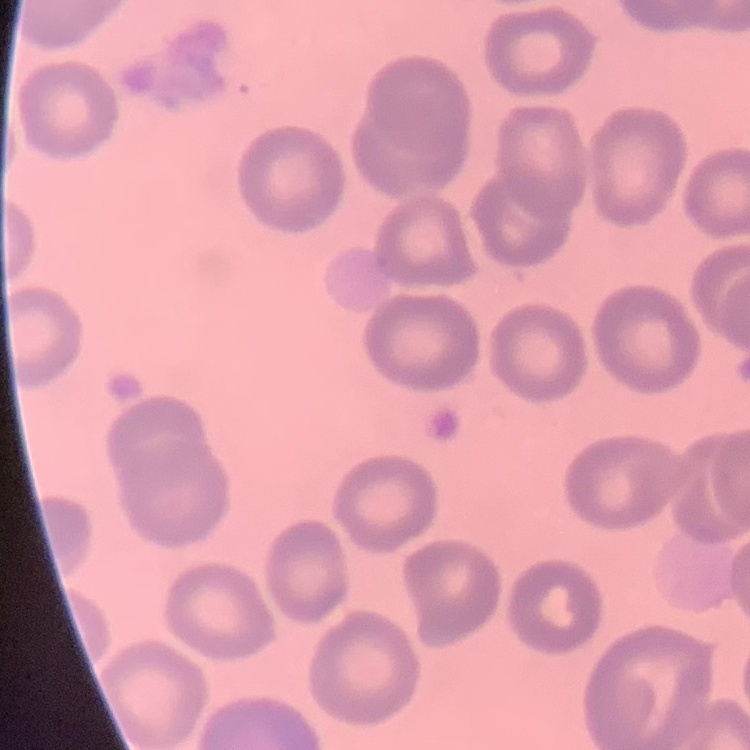
Summary:
  - Red blood cell morphology: no rouleaux formation
  - Image type: one tile cut from a larger photomicrograph
  - Preparation: thin blood smear
  - Stain: Field's or Giemsa